Assess this cell for malaria.
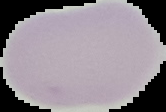

It is uninfected.

{
  "image_type": "cell region segmented out of the field of view; surrounding area masked to black",
  "preparation": "thin blood smear",
  "image_size": "166×112 pixels"
}